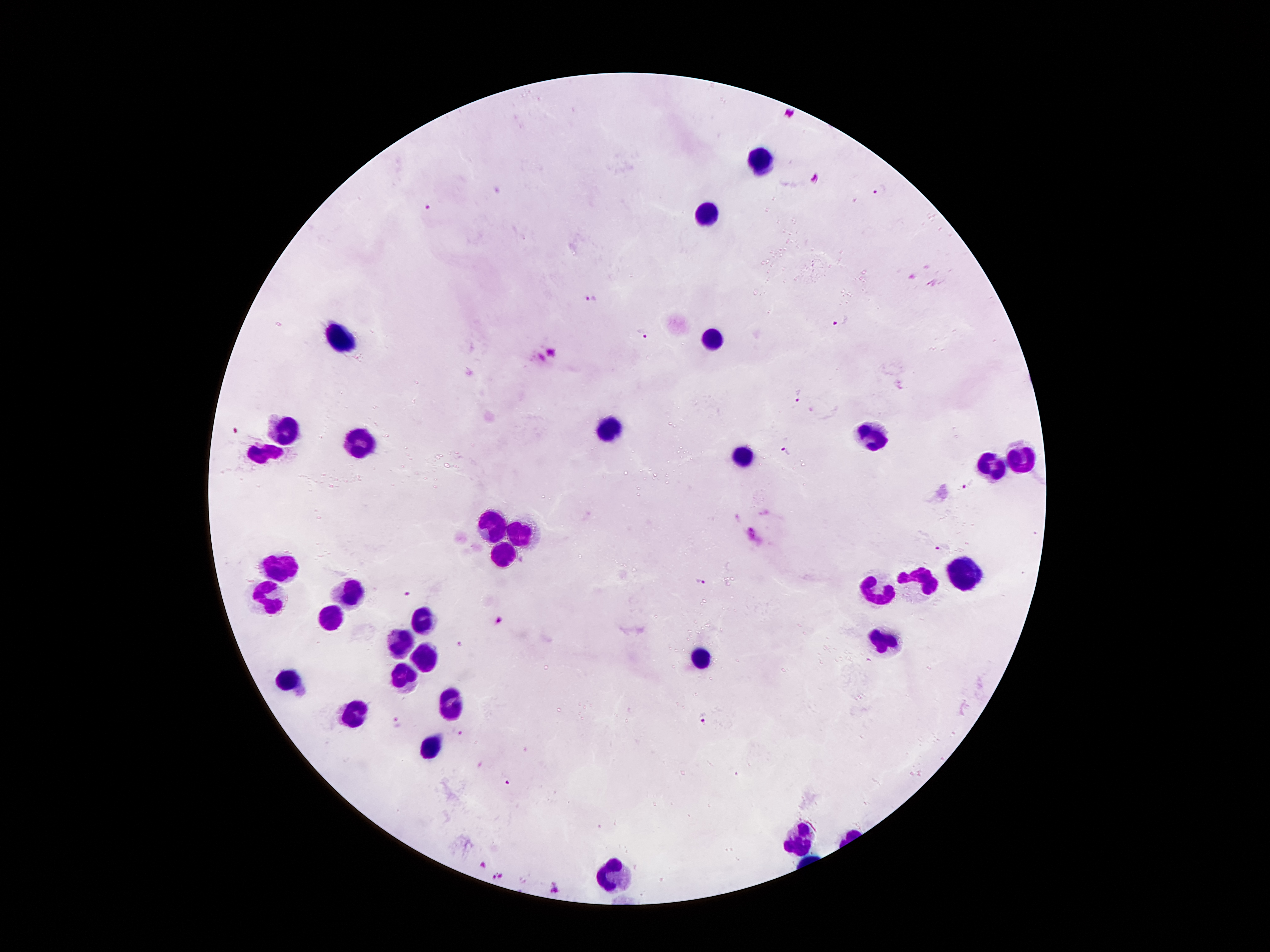 Approximate centers as (x, y) in pixels. Malaria parasite locations: (881, 192), (426, 208), (591, 298), (840, 321), (645, 334), (551, 351), (800, 394), (236, 434), (786, 452), (970, 484), (941, 548), (701, 582), (411, 593), (499, 620), (703, 719), (398, 722), (457, 732), (506, 781), (483, 865), (498, 877), (555, 888). Leukocyte locations: (757, 158), (707, 213), (340, 333), (715, 339), (287, 428), (609, 428), (872, 435), (357, 446), (267, 451), (743, 457), (1017, 462), (989, 465), (494, 527), (516, 533), (502, 554), (281, 563), (964, 571), (914, 583), (877, 589), (348, 591), (267, 593), (329, 618), (418, 622), (880, 641), (399, 642), (698, 659), (421, 660), (401, 677), (287, 678), (449, 702), (354, 712), (429, 748), (799, 836), (611, 875). Image is 1270×952 pixels. One field from this slide. 100x magnification. Thick blood film. Patient malaria status: positive for Plasmodium falciparum. Giemsa stain. Smartphone photograph taken through the microscope eyepiece.